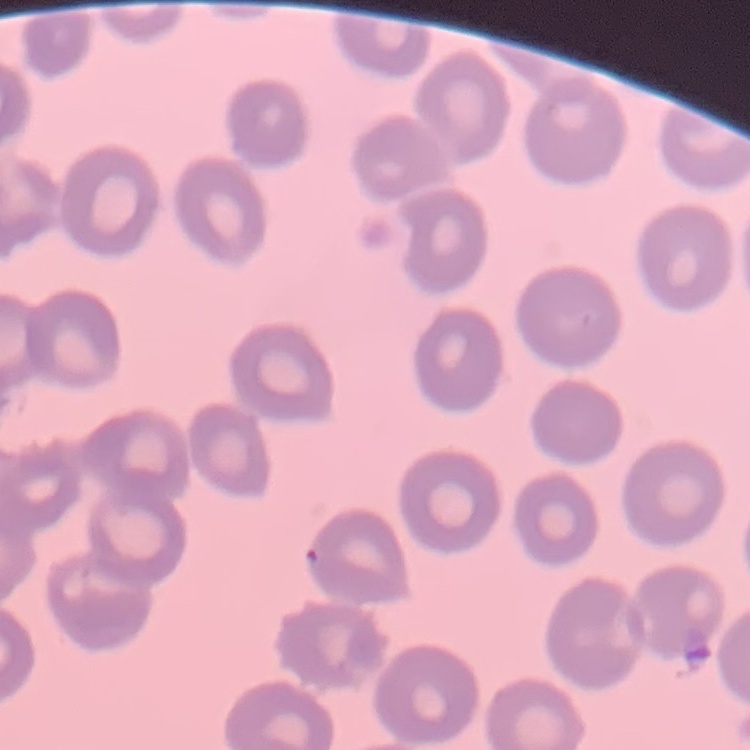
The erythrocytes show no rouleaux formation. Field's or Giemsa stain. Square crop of a larger photomicrograph. Thin blood smear.